Comment on the morphology of the erythrocytes.
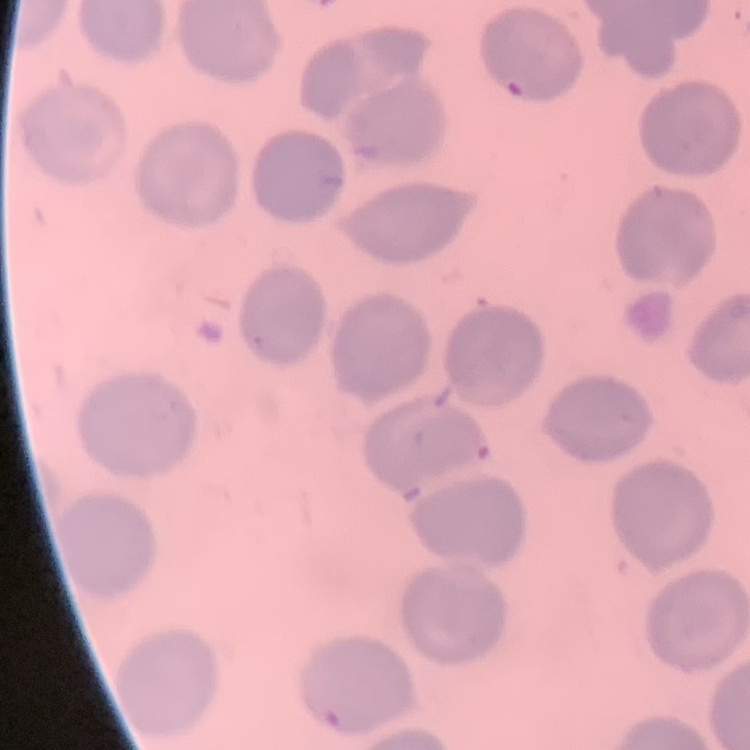
They show no rouleaux formation.

Summary:
  - Preparation: thin blood smear
  - Image type: square crop of a larger photomicrograph
  - Stain: Field's or Giemsa